Look for parasitized red blood cells.
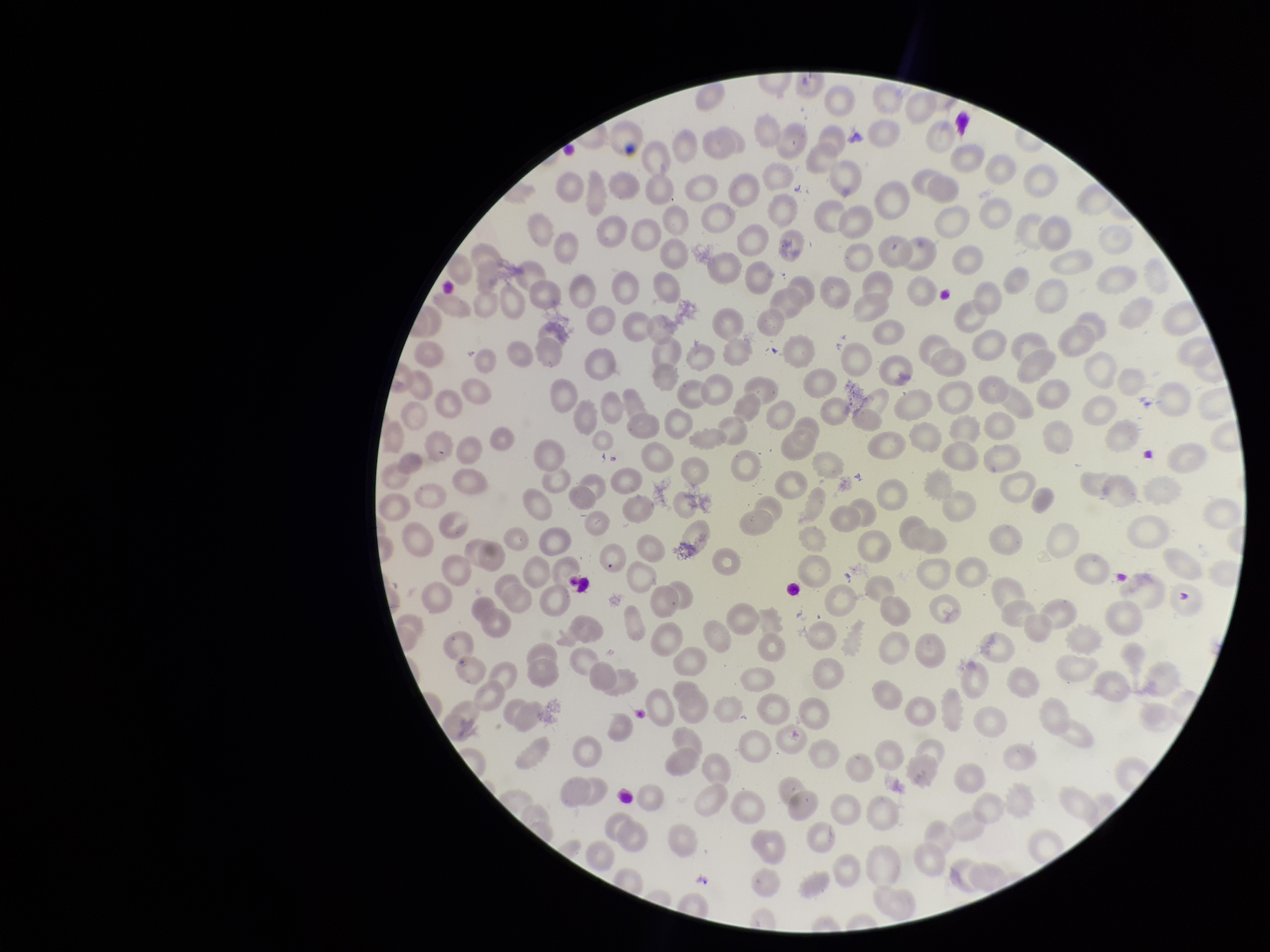
None seen.

Summary:
  - Field of view: one from this slide
  - Capture: smartphone photograph through the microscope eyepiece
  - Parasitized red blood cell count: 0
  - Red blood cell count: 230
  - Image size: 1270×952 pixels
  - Preparation: thin
  - Patient malaria status: positive
  - Stain: Giemsa
  - Species reported for this patient: Plasmodium falciparum